State the blood parasite species.
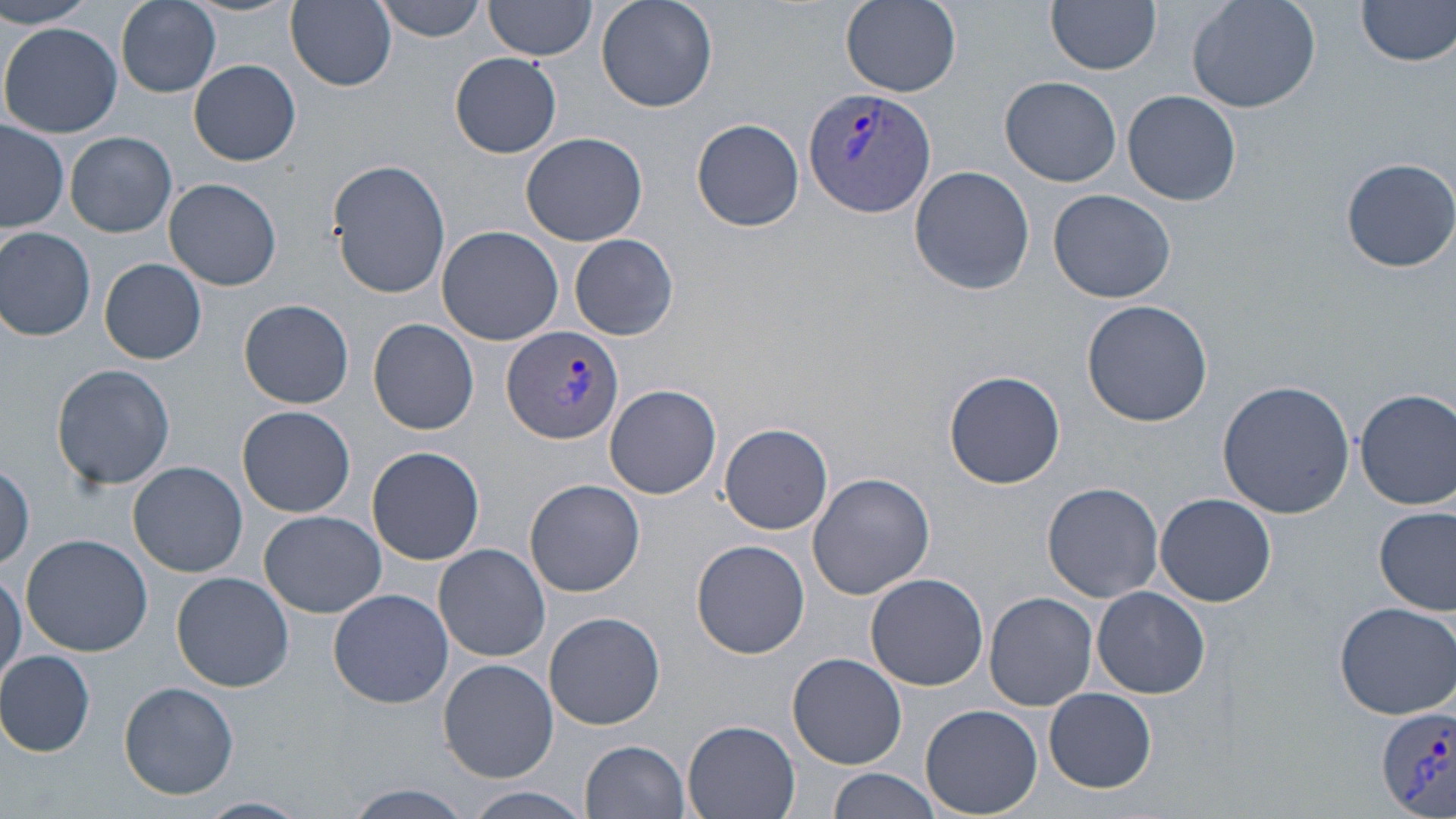
Plasmodium vivax.

Approximate bounding boxes as (x1, y1, x2, y2) in pixels. Plasmodium vivax-infected red blood cell locations: (802, 85, 936, 218), (503, 325, 624, 445), (1378, 705, 1456, 818). Uninfected red blood cell locations: (0, 0, 93, 28), (114, 0, 225, 100), (287, 0, 397, 91), (373, 0, 489, 41), (596, 0, 717, 113), (841, 0, 961, 95), (1047, 0, 1163, 74), (1185, 0, 1321, 112), (1355, 0, 1456, 67), (483, 1, 596, 63), (1, 24, 121, 138), (451, 53, 561, 158), (189, 59, 302, 166), (1000, 75, 1122, 187), (1122, 88, 1242, 205), (693, 118, 804, 232), (1, 121, 70, 233), (65, 131, 177, 237), (520, 132, 648, 246), (1341, 156, 1456, 273), (329, 160, 451, 299), (909, 165, 1034, 295), (163, 178, 283, 292), (1049, 188, 1176, 304), (437, 226, 565, 347), (0, 227, 97, 341), (570, 233, 678, 341), (100, 258, 205, 364), (239, 298, 354, 409), (1082, 299, 1214, 428), (369, 318, 479, 435), (51, 363, 177, 492), (944, 370, 1066, 489), (1216, 379, 1354, 519), (605, 384, 721, 498), (1355, 387, 1456, 509), (237, 405, 355, 517), (720, 423, 833, 533), (367, 446, 484, 566), (128, 461, 249, 578), (807, 471, 935, 599), (525, 479, 646, 597), (1042, 481, 1165, 602), (1155, 494, 1277, 606), (1374, 507, 1454, 617), (259, 509, 386, 618), (19, 532, 152, 657), (693, 540, 810, 659), (433, 543, 551, 662), (1, 571, 25, 689), (171, 572, 294, 692), (866, 573, 988, 691), (1092, 584, 1209, 699), (328, 589, 455, 710), (984, 592, 1098, 711), (1331, 600, 1456, 719), (545, 611, 666, 730), (0, 649, 96, 757), (787, 653, 907, 769), (439, 660, 559, 784), (119, 680, 239, 801), (1043, 688, 1157, 793), (921, 704, 1042, 819), (682, 719, 801, 819), (581, 739, 691, 819), (826, 769, 941, 819), (344, 783, 475, 818), (464, 787, 593, 817), (198, 795, 308, 819). 1000x magnification. One field of a larger specimen. May-Grünwald-Giemsa stain. Optical microscopy. Thin blood smear. Image is 1456×819 pixels.